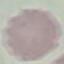
Malaria status: uninfected. Cell patch, automatically extracted from a larger field of view and resized to 64 × 64 pixels. Giemsa-stained preparation. Thin smear of blood. Acquired by smartphone through the microscope eyepiece.